Comment on the morphology of the red blood cells.
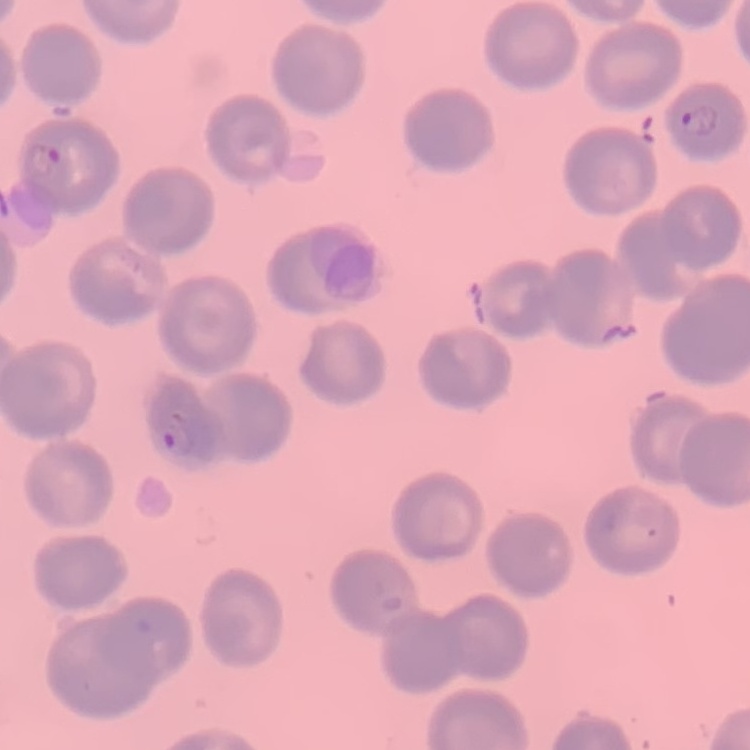
No rouleaux formation.

image type = square crop of a larger photomicrograph
preparation = thin blood smear
stain = Field's or Giemsa